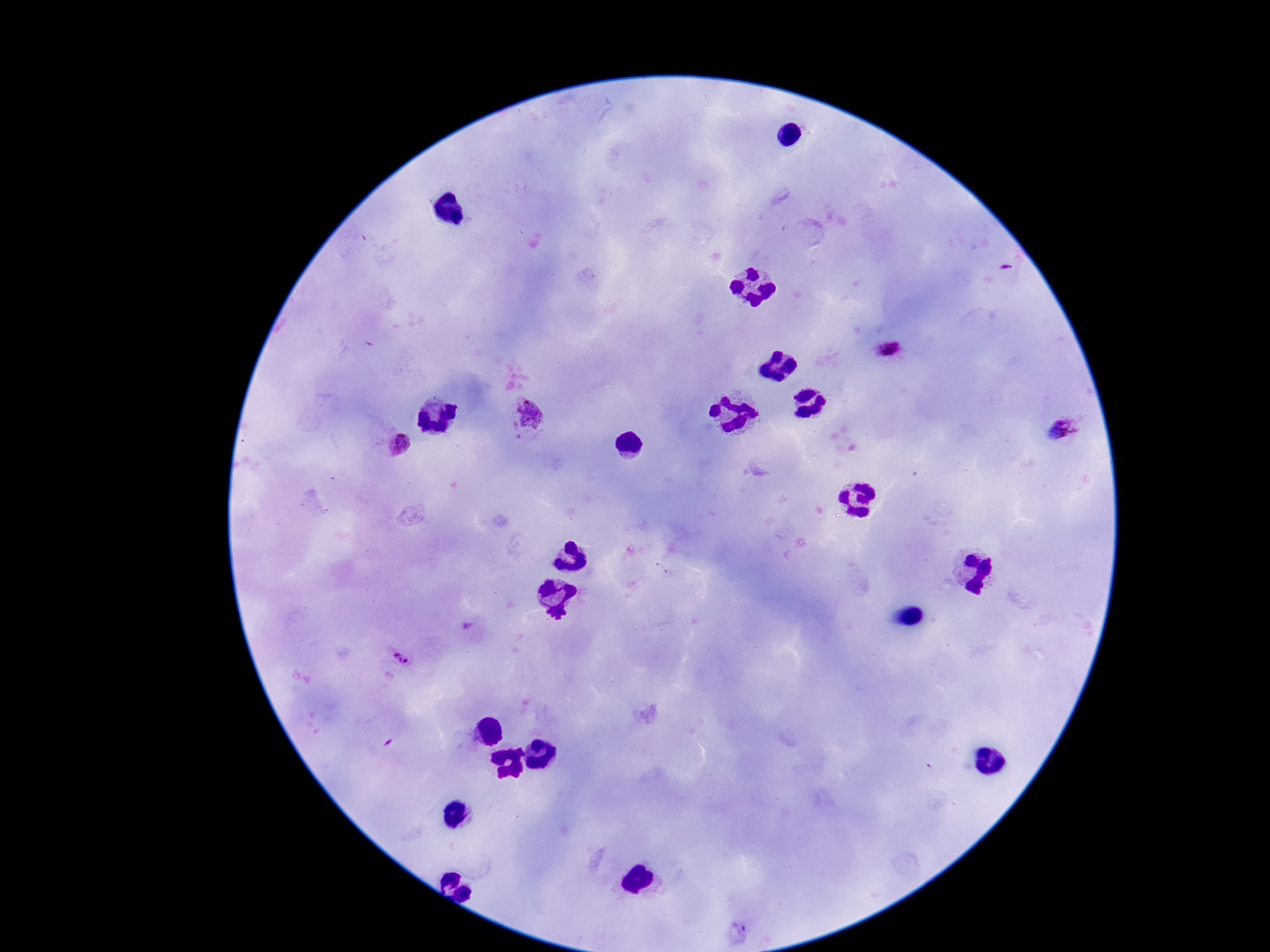
Approximate object centers, in pixels from the top-left corner.
Summary:
  - Plasmodium parasite locations: (x=1007, y=269), (x=888, y=351), (x=530, y=417), (x=1062, y=429), (x=397, y=444), (x=467, y=626), (x=399, y=657)
  - Preparation: thick blood smear
  - Image size: 1270×952 pixels
  - Patient malaria status: infected
  - Stain: Giemsa
  - Capture: smartphone camera through the microscope eyepiece
  - Magnification: 100x
  - Field of view: one from this slide